Assess the morphology of the erythrocytes.
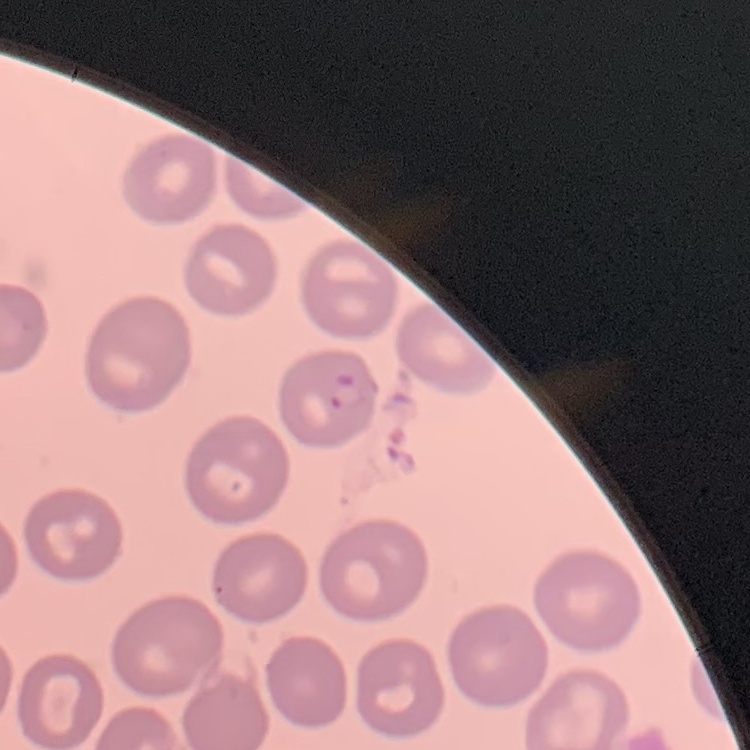

No rouleaux formation.

Thin blood film. One tile cut from a larger photomicrograph. Field's or Giemsa stain.